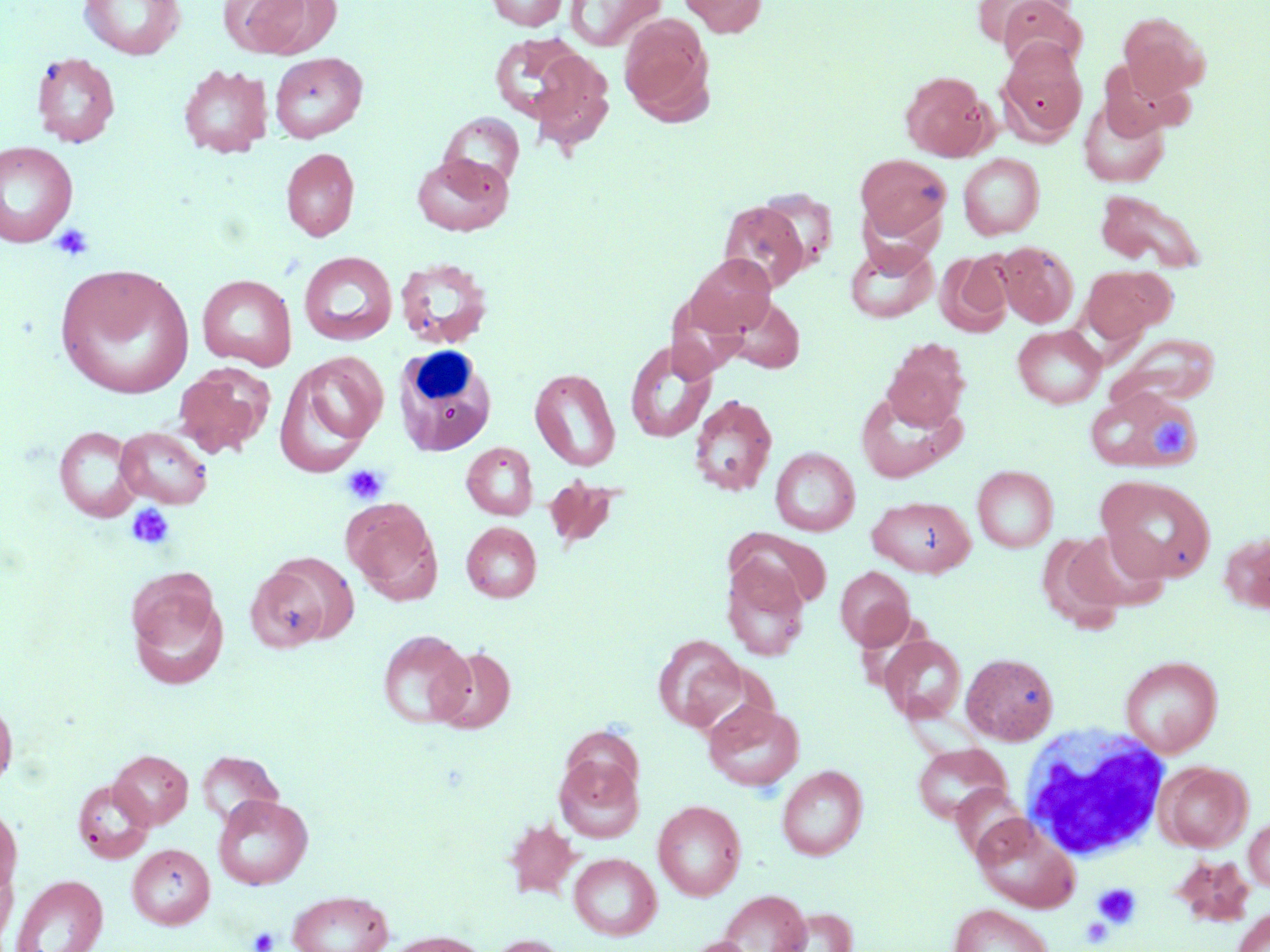
slide-level diagnosis = no evidence of blood parasites
uninfected red blood cell locations = approximate bounding boxes as named x1/y1/x2/y2 corners in pixels: (x1=78, y1=0, x2=186, y2=60), (x1=223, y1=0, x2=331, y2=57), (x1=486, y1=0, x2=569, y2=30), (x1=565, y1=0, x2=666, y2=51), (x1=680, y1=0, x2=765, y2=37), (x1=973, y1=0, x2=1068, y2=47), (x1=997, y1=0, x2=1085, y2=71), (x1=1118, y1=11, x2=1210, y2=99), (x1=618, y1=12, x2=714, y2=122), (x1=488, y1=34, x2=593, y2=124), (x1=519, y1=44, x2=615, y2=150), (x1=998, y1=44, x2=1087, y2=144), (x1=30, y1=52, x2=120, y2=148), (x1=269, y1=52, x2=368, y2=142), (x1=178, y1=64, x2=273, y2=158), (x1=900, y1=70, x2=994, y2=161), (x1=1078, y1=99, x2=1170, y2=187), (x1=438, y1=112, x2=525, y2=193), (x1=0, y1=141, x2=78, y2=248), (x1=281, y1=148, x2=360, y2=241), (x1=412, y1=153, x2=513, y2=236), (x1=957, y1=153, x2=1044, y2=240), (x1=856, y1=154, x2=951, y2=239), (x1=1094, y1=189, x2=1208, y2=273), (x1=718, y1=201, x2=809, y2=292), (x1=845, y1=241, x2=938, y2=324), (x1=995, y1=241, x2=1078, y2=327), (x1=299, y1=251, x2=397, y2=346), (x1=938, y1=251, x2=1013, y2=336), (x1=682, y1=253, x2=777, y2=339), (x1=395, y1=258, x2=494, y2=349), (x1=54, y1=263, x2=194, y2=399), (x1=1081, y1=264, x2=1173, y2=345), (x1=197, y1=274, x2=297, y2=371), (x1=719, y1=296, x2=806, y2=373), (x1=1012, y1=325, x2=1106, y2=408), (x1=1118, y1=333, x2=1222, y2=404), (x1=625, y1=340, x2=716, y2=444), (x1=883, y1=340, x2=970, y2=429), (x1=281, y1=352, x2=388, y2=468), (x1=173, y1=363, x2=274, y2=458), (x1=529, y1=368, x2=621, y2=471), (x1=1086, y1=388, x2=1201, y2=473), (x1=856, y1=391, x2=964, y2=482), (x1=689, y1=394, x2=778, y2=497), (x1=53, y1=425, x2=144, y2=523), (x1=114, y1=427, x2=213, y2=509), (x1=461, y1=442, x2=538, y2=520), (x1=770, y1=447, x2=860, y2=535), (x1=972, y1=465, x2=1058, y2=552), (x1=1097, y1=475, x2=1216, y2=585), (x1=543, y1=476, x2=623, y2=549), (x1=867, y1=496, x2=975, y2=577), (x1=343, y1=499, x2=442, y2=604), (x1=461, y1=522, x2=541, y2=602), (x1=1066, y1=528, x2=1169, y2=612), (x1=1220, y1=530, x2=1270, y2=615), (x1=1038, y1=534, x2=1126, y2=633), (x1=245, y1=555, x2=352, y2=651), (x1=722, y1=559, x2=810, y2=661), (x1=835, y1=566, x2=915, y2=649), (x1=126, y1=574, x2=229, y2=690), (x1=377, y1=629, x2=474, y2=729), (x1=880, y1=634, x2=966, y2=724), (x1=653, y1=635, x2=746, y2=732), (x1=432, y1=646, x2=516, y2=734), (x1=961, y1=652, x2=1059, y2=745), (x1=1120, y1=655, x2=1222, y2=756), (x1=0, y1=693, x2=17, y2=793), (x1=703, y1=700, x2=804, y2=791), (x1=914, y1=743, x2=1009, y2=823), (x1=109, y1=750, x2=193, y2=829), (x1=197, y1=750, x2=283, y2=828), (x1=554, y1=755, x2=644, y2=843), (x1=1156, y1=761, x2=1252, y2=852), (x1=777, y1=766, x2=868, y2=861), (x1=72, y1=778, x2=155, y2=862), (x1=952, y1=784, x2=1029, y2=861), (x1=213, y1=794, x2=313, y2=890), (x1=653, y1=799, x2=746, y2=901), (x1=0, y1=804, x2=22, y2=897), (x1=1243, y1=815, x2=1270, y2=892), (x1=973, y1=816, x2=1079, y2=913), (x1=503, y1=818, x2=580, y2=900), (x1=127, y1=844, x2=215, y2=930), (x1=568, y1=852, x2=661, y2=940), (x1=0, y1=861, x2=17, y2=947), (x1=10, y1=874, x2=108, y2=952), (x1=718, y1=889, x2=810, y2=952), (x1=287, y1=890, x2=394, y2=952), (x1=948, y1=904, x2=1053, y2=952), (x1=774, y1=907, x2=857, y2=952), (x1=1233, y1=907, x2=1270, y2=952), (x1=383, y1=931, x2=489, y2=952), (x1=486, y1=934, x2=569, y2=952), (x1=683, y1=937, x2=756, y2=952)
stain = May-Grünwald-Giemsa
image size = 1270×952 pixels
preparation = thin blood film
modality = optical microscopy
platelet locations = approximate bounding boxes as named x1/y1/x2/y2 corners in pixels: (x1=49, y1=222, x2=95, y2=262), (x1=1154, y1=419, x2=1193, y2=459), (x1=341, y1=463, x2=389, y2=505), (x1=125, y1=502, x2=176, y2=551), (x1=1093, y1=883, x2=1141, y2=927), (x1=1081, y1=917, x2=1112, y2=948), (x1=248, y1=926, x2=279, y2=952)
magnification = 1000x
field of view = single
white blood cell locations = approximate bounding boxes as named x1/y1/x2/y2 corners in pixels: (x1=393, y1=345, x2=498, y2=458), (x1=1019, y1=724, x2=1173, y2=862)